Locate every malaria parasite.
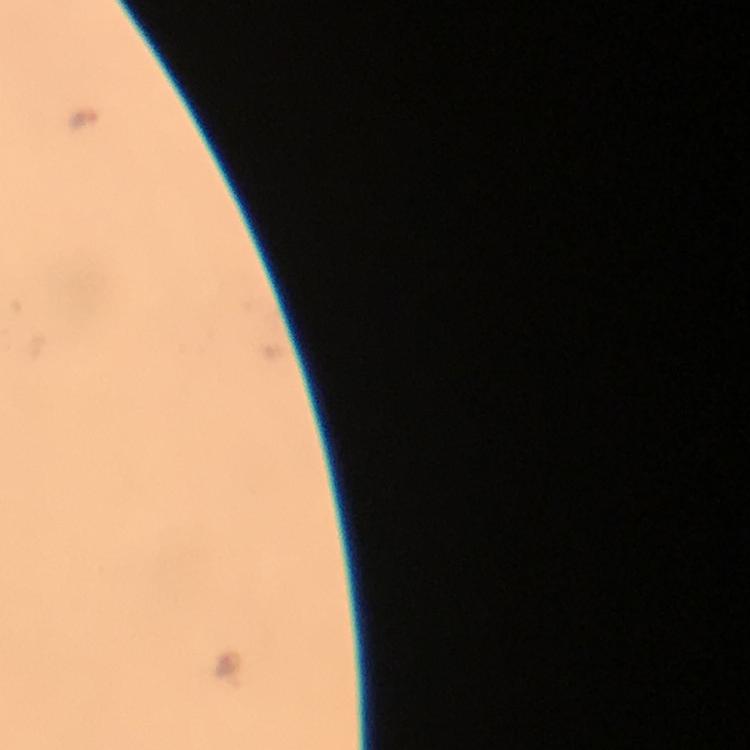
Approximate centers as (x, y) in pixels.
Malaria parasites: (82, 119).

magnification = 100x
stain = Giemsa
image size = 750×750 pixels
context = from a diagnostic examination for malaria
immersion oil = used
cropped from = one field of view
capture = smartphone photograph through a microscope
preparation = thick blood film